Point out each leukocyte.
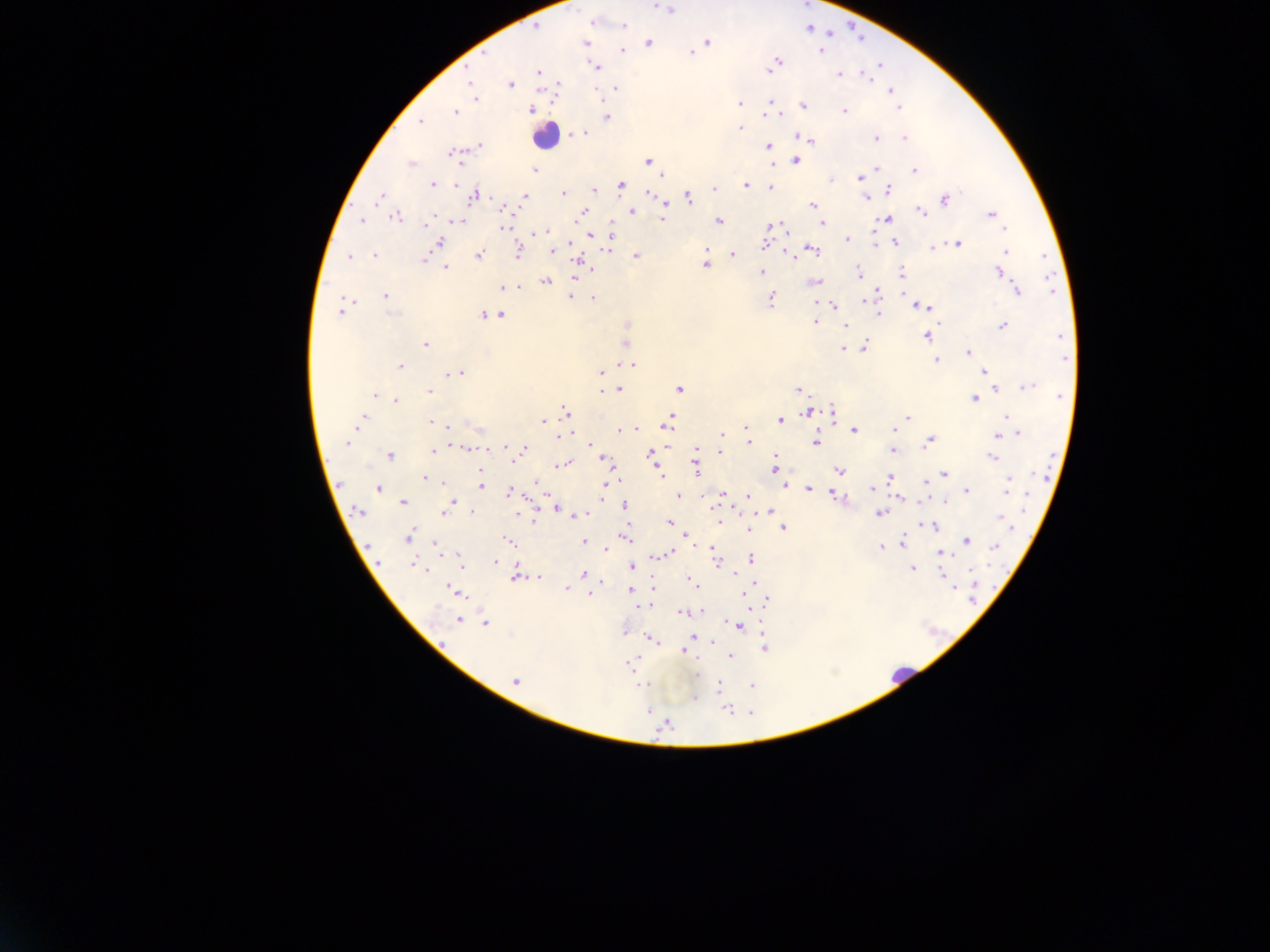

Approximate centers as [x, y] in pixels.
Leukocytes: [545, 136], [903, 675].

{
  "image_size": "1270×952 pixels",
  "capture": "mobile-phone photograph through a microscope",
  "preparation": "thick blood film",
  "country": "Ghana",
  "plasmodium_parasite_locations": "approximate centers as [x, y] in pixels: [655, 5], [668, 8], [593, 22], [624, 24], [535, 28], [707, 41], [586, 43], [648, 43], [819, 50], [623, 51], [693, 52], [778, 61], [772, 66], [597, 67], [538, 72], [839, 74], [867, 77], [469, 80], [510, 84], [616, 89], [892, 91], [475, 97], [894, 97], [739, 103], [803, 105], [899, 107], [531, 110], [770, 110], [844, 111], [455, 112], [775, 113], [607, 117], [421, 121], [740, 128], [577, 134], [583, 134], [905, 137], [875, 138], [809, 140], [479, 146], [769, 147], [454, 154], [648, 160], [796, 161], [410, 163], [773, 163], [876, 168], [915, 170], [534, 171], [860, 177], [830, 180], [432, 183], [455, 183], [621, 184], [746, 185], [770, 187], [713, 188], [889, 190], [594, 191], [563, 193], [648, 194], [474, 196], [524, 196], [688, 197], [866, 197], [379, 198], [945, 199], [813, 205], [501, 209], [662, 209], [582, 211], [632, 211], [920, 211], [991, 214], [396, 217], [662, 218], [433, 219], [887, 219], [362, 220], [718, 221], [458, 222], [426, 223], [611, 224], [823, 224], [772, 225], [504, 227], [1004, 228], [543, 231], [591, 236], [847, 239], [439, 242], [894, 242], [765, 243], [957, 244], [932, 247], [553, 249], [606, 250], [813, 250], [519, 251], [1005, 251], [706, 252], [374, 255], [479, 255], [733, 255], [636, 256], [350, 257], [423, 259], [580, 263], [704, 265], [446, 267], [590, 270], [762, 272], [858, 272], [998, 272], [902, 273], [575, 278], [545, 282], [815, 282], [503, 287], [515, 287], [1016, 291], [384, 295], [875, 295], [569, 297], [593, 299], [771, 300], [834, 305], [342, 307], [924, 307], [878, 314], [393, 315], [482, 316], [501, 316], [815, 322], [627, 325], [1002, 325], [845, 326], [926, 336], [625, 343], [425, 344], [864, 347], [843, 348], [968, 351], [937, 360], [632, 364], [400, 366], [984, 372], [460, 373], [601, 373], [1030, 386], [619, 389], [680, 389], [798, 389], [996, 390], [430, 392], [374, 396], [1059, 396], [974, 399], [396, 401], [833, 411], [566, 412], [807, 413], [1006, 416], [907, 417], [361, 418], [780, 421], [431, 422], [543, 422], [668, 423], [446, 426], [746, 428], [620, 430], [894, 430], [854, 431], [722, 434], [1017, 434], [562, 435], [998, 436], [749, 441], [816, 442], [929, 442], [347, 443], [591, 445], [505, 447], [464, 449], [523, 450], [697, 450], [893, 450], [432, 451], [720, 452], [650, 455], [390, 456], [991, 457], [514, 458], [602, 458], [696, 461], [775, 461], [564, 465], [774, 468], [697, 470], [839, 470], [944, 474], [661, 475], [424, 478], [891, 478], [1009, 481], [443, 483], [926, 483], [481, 484], [536, 485], [784, 486], [605, 487], [872, 488], [378, 489], [809, 489], [1007, 490], [967, 491], [510, 492], [722, 494], [678, 495], [835, 495], [749, 497], [944, 502], [403, 503], [450, 505], [625, 506], [557, 508], [359, 511], [770, 511], [444, 512], [473, 513], [879, 513], [580, 515], [1001, 519], [534, 520], [719, 521], [669, 523], [932, 525], [783, 528], [748, 529], [685, 535], [408, 536], [626, 537], [509, 541], [583, 541], [967, 541], [902, 542], [435, 544], [880, 547], [995, 547], [607, 549], [667, 554], [942, 554], [662, 555], [750, 558], [715, 559], [460, 560], [494, 562], [414, 564], [631, 566], [913, 569], [584, 573], [943, 575], [516, 577], [539, 578], [691, 581], [653, 587], [566, 589], [630, 589], [453, 590], [591, 593], [745, 594], [768, 600], [649, 605], [643, 606], [683, 613], [458, 620], [485, 624], [738, 626], [624, 633], [697, 639], [652, 640], [765, 649], [684, 652], [730, 656], [632, 661], [697, 674], [515, 682], [641, 685], [751, 685], [718, 688], [694, 697], [728, 709], [649, 712], [666, 725]",
  "field_of_view": "single"
}